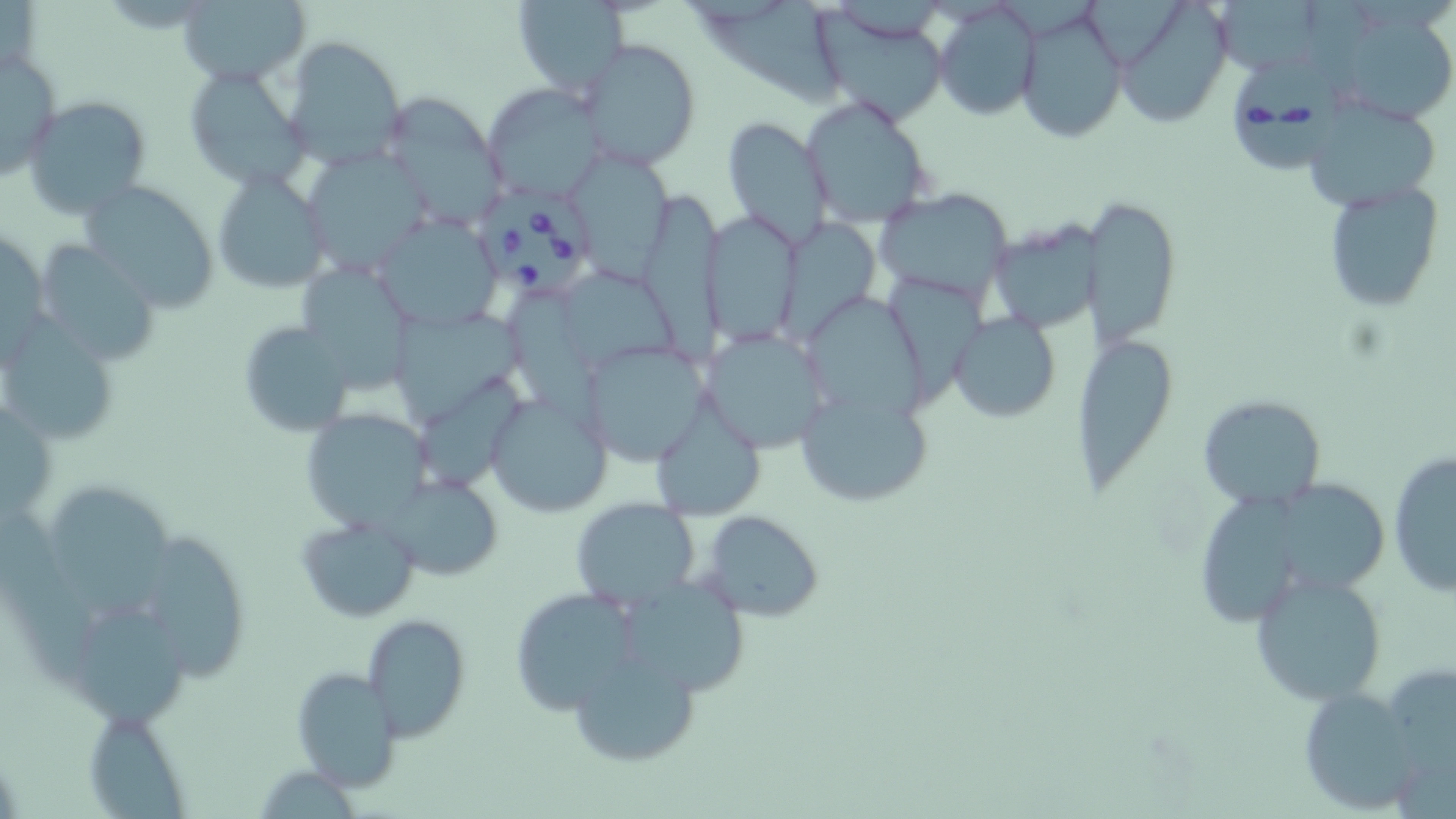 Approximate bounding boxes as (x1, y1, x2, y2) in pixels. Babesia divergens-infected red blood cell locations: (1230, 53, 1344, 174), (471, 188, 595, 299). Uninfected red blood cell locations: (1087, 0, 1188, 72), (1219, 0, 1319, 76), (178, 1, 309, 86), (512, 1, 629, 94), (1125, 1, 1235, 130), (933, 3, 1043, 122), (1017, 5, 1129, 144), (704, 6, 847, 113), (815, 6, 955, 123), (1353, 20, 1451, 125), (576, 36, 700, 171), (281, 37, 407, 171), (0, 47, 61, 181), (182, 62, 310, 192), (481, 84, 604, 200), (379, 92, 508, 234), (24, 96, 153, 220), (799, 96, 936, 229), (1301, 97, 1444, 213), (720, 115, 834, 248), (300, 147, 436, 274), (575, 152, 674, 289), (213, 169, 331, 294), (78, 179, 221, 311), (1320, 180, 1445, 312), (873, 187, 1017, 303), (640, 193, 730, 367), (1079, 197, 1180, 347), (707, 210, 808, 347), (375, 214, 503, 332), (988, 215, 1111, 332), (777, 218, 881, 342), (35, 239, 164, 368), (303, 265, 418, 394), (568, 274, 682, 373), (889, 275, 990, 401), (807, 290, 932, 424), (510, 294, 607, 443), (950, 311, 1061, 423), (393, 316, 529, 425), (1, 318, 120, 448), (236, 320, 352, 438), (701, 327, 827, 452), (1079, 339, 1173, 498), (581, 341, 712, 464), (798, 386, 931, 509), (484, 392, 614, 519), (1196, 394, 1327, 511), (300, 407, 434, 530), (652, 410, 765, 519), (1387, 450, 1456, 599), (382, 472, 503, 581), (1280, 478, 1390, 599), (50, 486, 179, 618), (1198, 488, 1306, 618), (569, 497, 700, 609), (700, 511, 823, 622), (295, 512, 420, 623), (3, 521, 96, 696), (147, 530, 249, 683), (1248, 570, 1390, 706), (621, 583, 753, 696), (508, 586, 637, 715), (79, 613, 195, 740), (361, 613, 471, 741), (570, 651, 701, 770), (289, 666, 403, 793), (1294, 686, 1432, 815), (83, 708, 191, 817). Slide-level diagnosis: Babesia divergens. One field of a larger specimen. 1000x magnification. Image is 1456×819 pixels. Light microscopy. May-Grünwald-Giemsa-stained preparation. Thin blood smear.